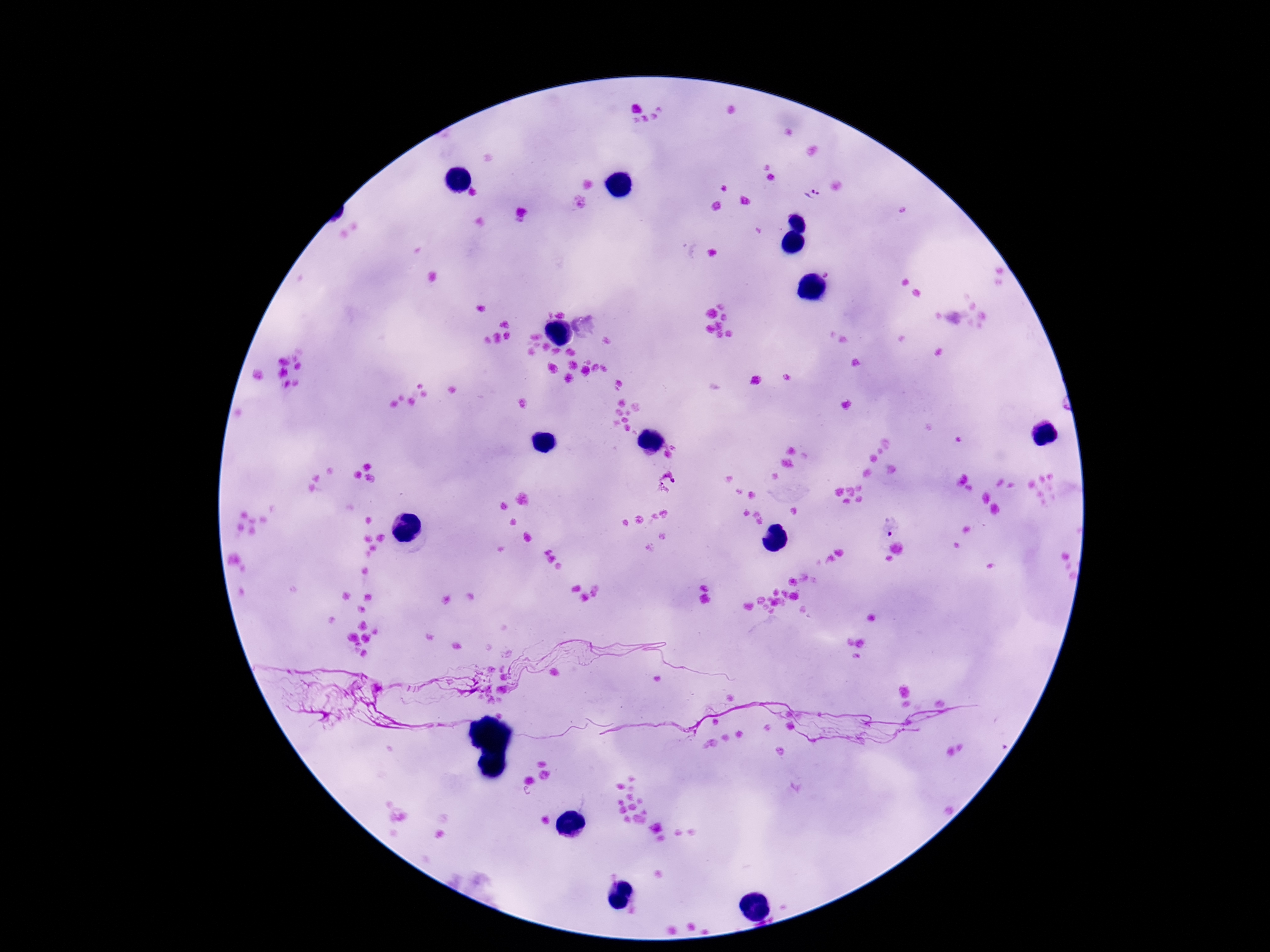
Approximate centers as {x, y} in pixels.
Summary:
  - Plasmodium parasite locations: {814, 195}, {671, 492}, {890, 525}
  - Field of view: single
  - Patient malaria status: infected
  - Capture: smartphone camera through the microscope eyepiece
  - Magnification: 100x
  - Stain: Giemsa
  - Image size: 1270×952 pixels
  - Preparation: thick blood film